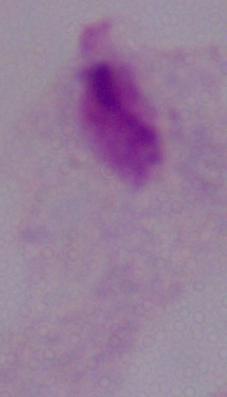
Summary:
  - Modality: photomicrograph
  - Magnification: 1000x
  - Identification: trichomonad